Comment on the morphology of the red blood cells.
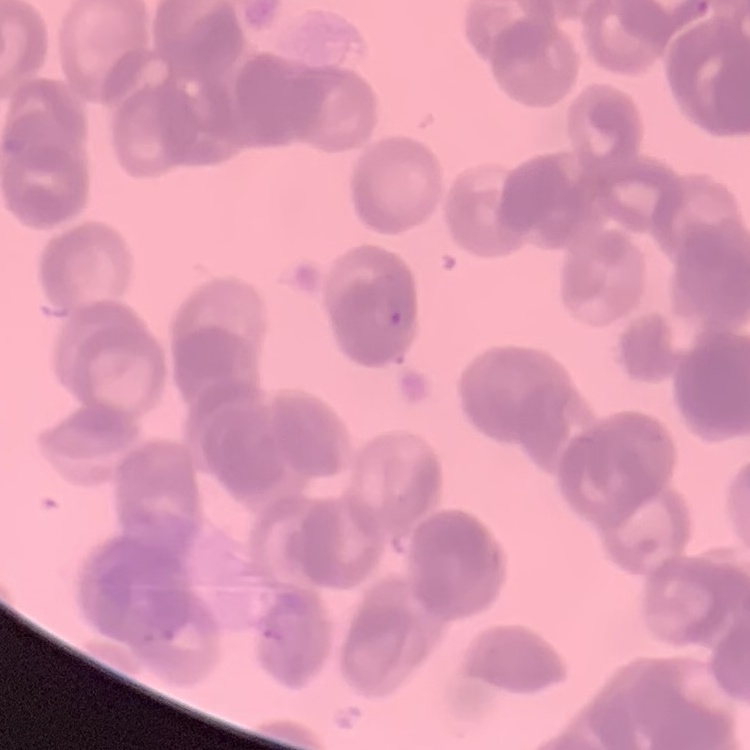
They show rouleaux formation.

Thin blood film. One tile cut from a larger photomicrograph. Field's or Giemsa stain.